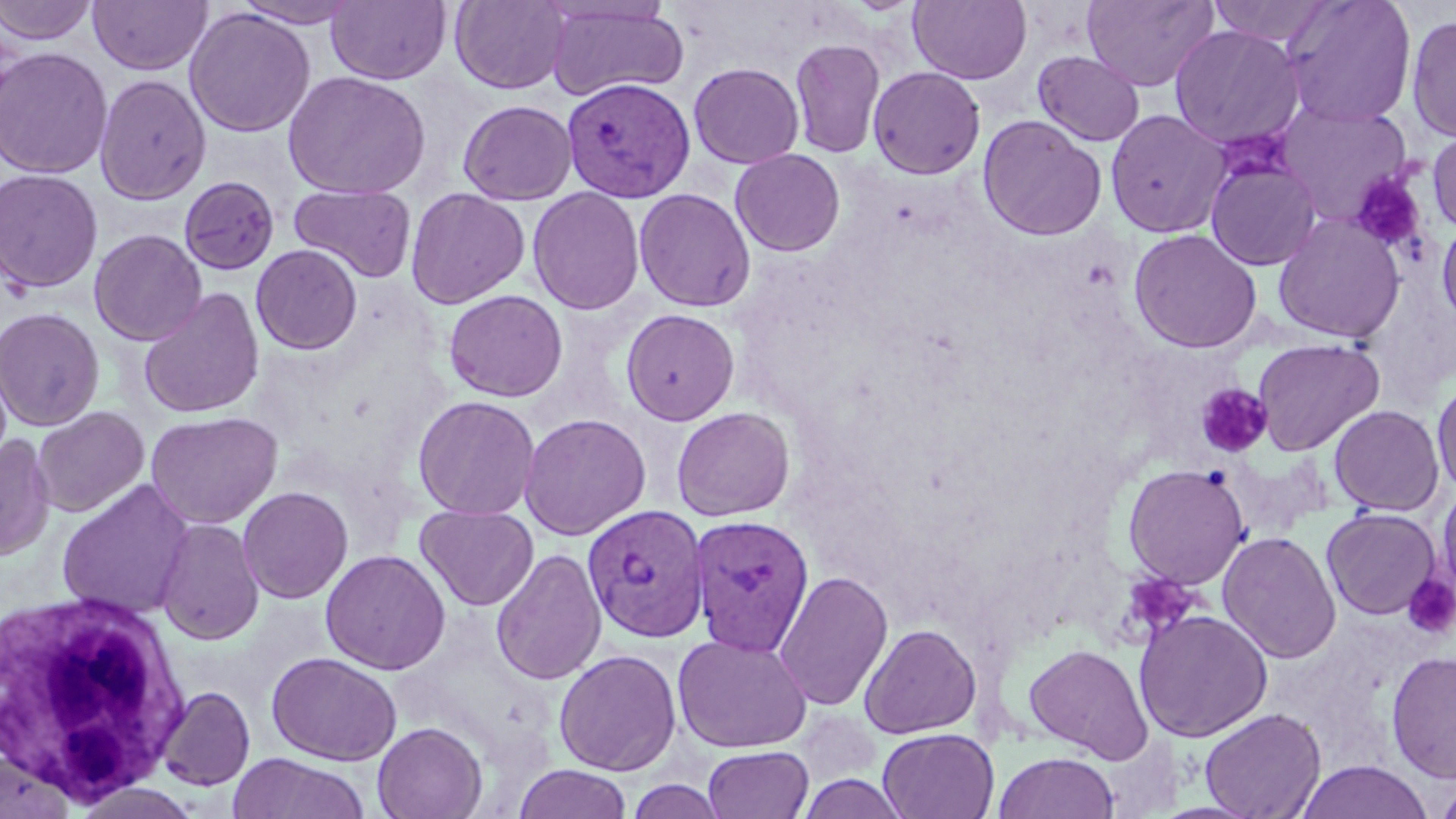
{
  "plasmodium_vivax_infected_red_blood_cell_locations": "approximate bounding boxes as (x1,y1)-(x2,y2) corner pairs in pixels: (561,77)-(696,202), (582,503)-(709,642), (688,514)-(815,656)",
  "slide_level_diagnosis": "Plasmodium vivax",
  "white_blood_cell_locations": "approximate bounding boxes as (x1,y1)-(x2,y2) corner pairs in pixels: (1,585)-(190,805)",
  "modality": "optical microscopy",
  "preparation": "thin blood film",
  "stain": "May-Grünwald-Giemsa",
  "image_size": "1456×819 pixels",
  "field_of_view": "single",
  "magnification": "1000x",
  "platelet_locations": "approximate bounding boxes as (x1,y1)-(x2,y2) corner pairs in pixels: (1350,171)-(1426,254), (1194,383)-(1272,456), (1123,573)-(1201,636), (1403,574)-(1456,639)",
  "uninfected_red_blood_cell_locations": "approximate bounding boxes as (x1,y1)-(x2,y2) corner pairs in pixels: (0,0)-(99,45), (88,0)-(212,76), (228,0)-(366,28), (909,0)-(1032,84), (1081,0)-(1219,91), (1207,0)-(1336,47), (326,1)-(452,85), (450,1)-(571,94), (1281,1)-(1418,127), (543,3)-(690,102), (184,7)-(316,138), (1405,13)-(1456,145), (1169,24)-(1305,150), (789,38)-(886,159), (0,47)-(113,179), (1032,51)-(1145,146), (688,62)-(805,168), (867,66)-(986,179), (283,71)-(431,199), (94,73)-(212,205), (458,99)-(578,205), (1276,102)-(1413,226), (1105,109)-(1232,239), (977,114)-(1106,241), (1427,129)-(1456,236), (730,149)-(846,257), (1205,155)-(1321,271), (0,168)-(104,294), (178,176)-(280,275), (289,184)-(417,283), (405,187)-(530,309), (527,187)-(645,315), (633,188)-(756,312), (1273,214)-(1406,344), (1436,216)-(1456,330), (88,228)-(207,346), (1128,228)-(1262,353), (251,244)-(362,354), (138,287)-(265,418), (443,289)-(568,402), (0,306)-(105,431), (621,308)-(740,426), (1252,338)-(1385,455), (1431,376)-(1456,499), (412,395)-(541,520), (1328,404)-(1445,516), (32,406)-(149,517), (671,406)-(796,522), (145,411)-(283,528), (519,412)-(651,540), (0,434)-(55,561), (1122,463)-(1250,589), (56,480)-(195,620), (1437,484)-(1456,599), (237,486)-(354,604), (416,504)-(539,611), (1321,507)-(1442,620), (155,517)-(264,645), (1217,530)-(1341,664), (491,548)-(607,686), (320,549)-(451,675), (773,570)-(894,712), (1133,608)-(1273,743), (860,623)-(982,739), (672,633)-(812,754), (1023,644)-(1154,762), (554,648)-(682,776), (266,651)-(402,766), (1385,651)-(1456,782), (157,686)-(255,791), (1199,707)-(1326,818), (372,721)-(487,819), (878,728)-(999,818), (703,745)-(814,819), (0,751)-(75,819), (993,751)-(1119,819), (226,753)-(369,819), (1295,760)-(1433,819), (513,764)-(633,819), (1433,773)-(1456,819), (798,774)-(907,819), (68,781)-(205,819)"
}